Identify the blood parasite species.
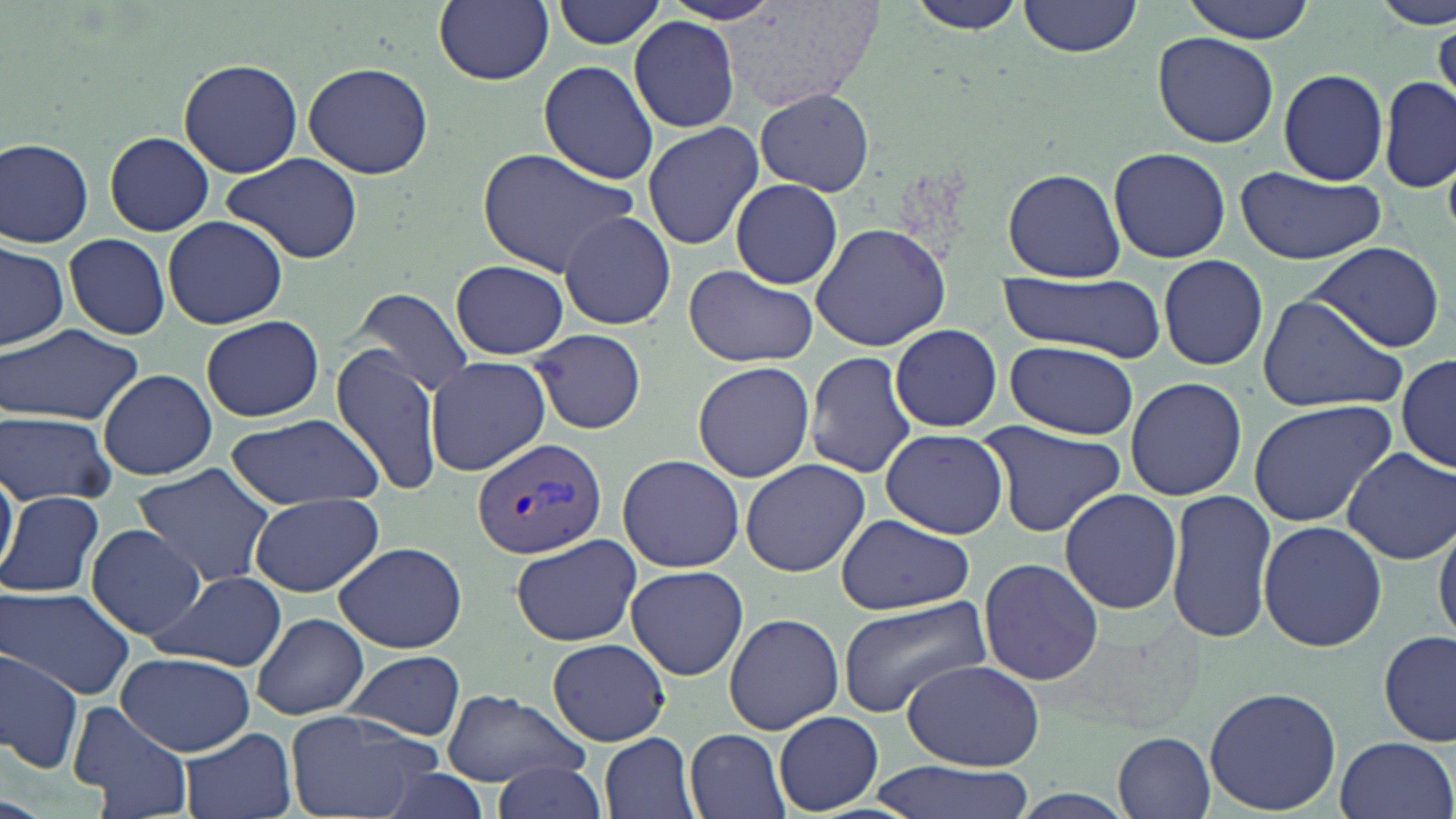
Plasmodium vivax.

Approximate bounding boxes as (x1, y1, x2, y2) in pixels. Uninfected red blood cell locations: (1020, 0, 1142, 57), (1181, 0, 1316, 42), (1374, 0, 1452, 27), (434, 1, 553, 86), (551, 1, 666, 51), (719, 1, 879, 115), (901, 1, 1029, 37), (630, 16, 742, 132), (1432, 22, 1455, 110), (1152, 30, 1279, 148), (178, 59, 302, 177), (538, 60, 659, 185), (302, 61, 435, 179), (1279, 69, 1389, 185), (1378, 76, 1455, 193), (754, 88, 875, 196), (642, 121, 764, 250), (104, 132, 214, 235), (0, 137, 94, 246), (1107, 146, 1232, 263), (476, 149, 640, 275), (221, 151, 366, 265), (1235, 167, 1387, 265), (1001, 169, 1125, 281), (730, 179, 845, 289), (559, 211, 677, 329), (162, 216, 289, 330), (810, 221, 953, 353), (63, 233, 170, 341), (0, 240, 68, 351), (1304, 241, 1447, 353), (1157, 255, 1267, 369), (451, 260, 568, 359), (684, 263, 821, 366), (999, 272, 1168, 363), (354, 288, 474, 397), (1254, 293, 1409, 415), (201, 315, 324, 422), (890, 323, 1002, 432), (0, 325, 143, 425), (527, 328, 648, 436), (1006, 340, 1139, 438), (331, 347, 447, 498), (804, 350, 917, 477), (423, 354, 553, 476), (1397, 354, 1456, 473), (692, 360, 815, 483), (97, 369, 218, 481), (1124, 376, 1247, 501), (1247, 400, 1397, 526), (0, 411, 117, 507), (224, 413, 384, 508), (977, 421, 1127, 536), (879, 428, 1008, 539), (1003, 441, 1168, 596), (1342, 446, 1456, 565), (615, 454, 745, 571), (739, 459, 871, 577), (0, 465, 17, 579), (131, 465, 279, 587), (1056, 488, 1182, 614), (1, 489, 105, 598), (1165, 490, 1278, 646), (249, 492, 384, 597), (834, 513, 977, 616), (1434, 514, 1456, 648), (1256, 519, 1388, 652), (86, 524, 205, 640), (510, 535, 643, 646), (334, 541, 468, 654), (979, 557, 1104, 686), (624, 564, 748, 681), (146, 569, 287, 672), (0, 588, 134, 698), (839, 592, 996, 716), (724, 612, 845, 734), (251, 613, 368, 719), (1380, 631, 1455, 748), (548, 637, 671, 746), (340, 649, 467, 740), (0, 651, 82, 773), (117, 653, 257, 756), (899, 659, 1045, 769), (1204, 685, 1342, 815), (440, 690, 588, 788), (71, 699, 192, 819), (284, 709, 445, 819), (773, 711, 883, 813), (180, 728, 298, 819), (683, 728, 791, 819), (600, 733, 700, 819), (1116, 733, 1217, 818), (1334, 734, 1454, 819), (868, 758, 1038, 819), (492, 761, 606, 819), (0, 796, 48, 819). Plasmodium vivax-infected red blood cell locations: (470, 435, 608, 561). Image is 1456×819 pixels. One field of a larger specimen. May-Grünwald-Giemsa stain. Optical microscopy. Thin blood film. Captured at 1000x magnification.